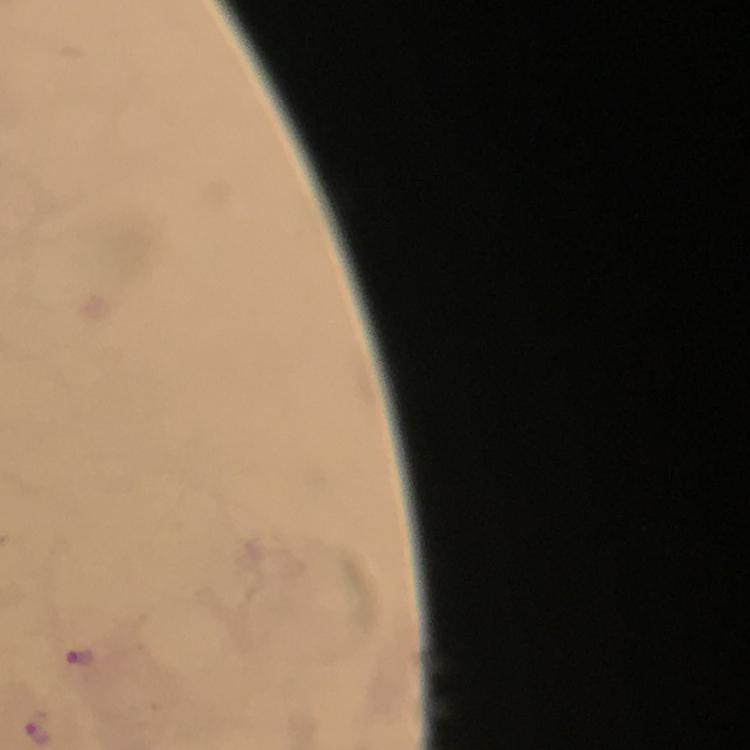
magnification = 100x
capture = smartphone photograph through a microscope
preparation = thick smear
immersion oil = applied
image size = 750×750 pixels
Plasmodium parasite locations = approximate centers as [x, y] in pixels: [77, 658]
context = from a malaria diagnostic workup
stain = Giemsa
cropped from = one field of view